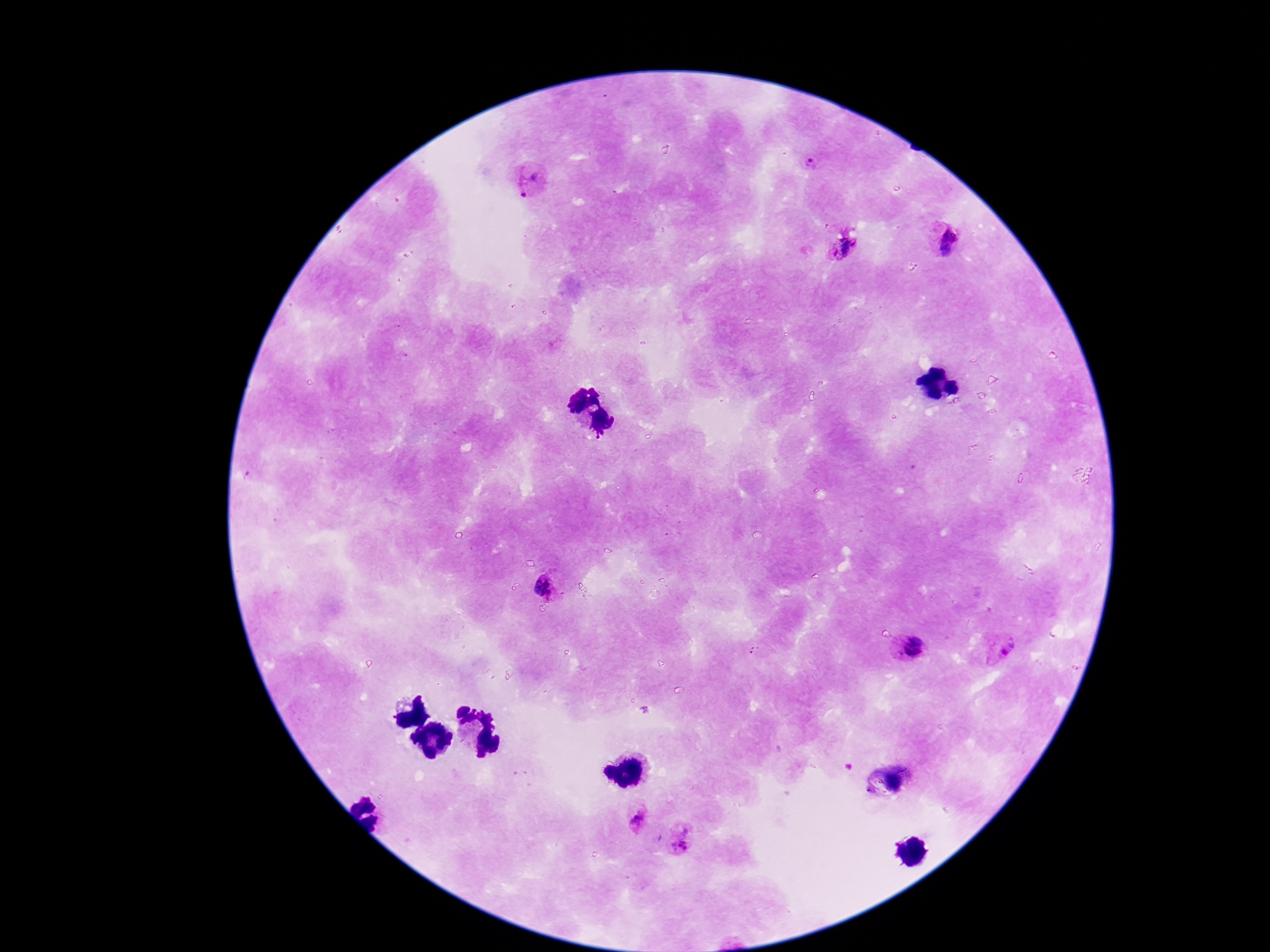

Approximate centers as {x, y} in pixels. Plasmodium parasite locations: {807, 164}, {529, 183}, {948, 241}, {845, 247}, {546, 587}, {1001, 647}, {913, 648}, {895, 780}, {636, 819}, {682, 837}. Photographed through the microscope eyepiece with a smartphone camera. 100x magnification. Giemsa stain. Single field of view. Image is 1270×952 pixels. Patient malaria status: positive. Thick blood smear.